Assess this cell for malaria.
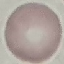

It is uninfected.

Summary:
  - Preparation: thin smear
  - Stain: Giemsa
  - Capture: smartphone camera at the microscope eyepiece
  - Image type: cell patch, automatically extracted from a larger field of view and resized to 64 × 64 pixels